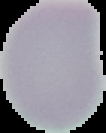
{
  "image_size": "106×133 pixels",
  "preparation": "thin blood film",
  "malaria_status": "uninfected",
  "image_type": "segmented cell region on a black background"
}